Report the malaria status.
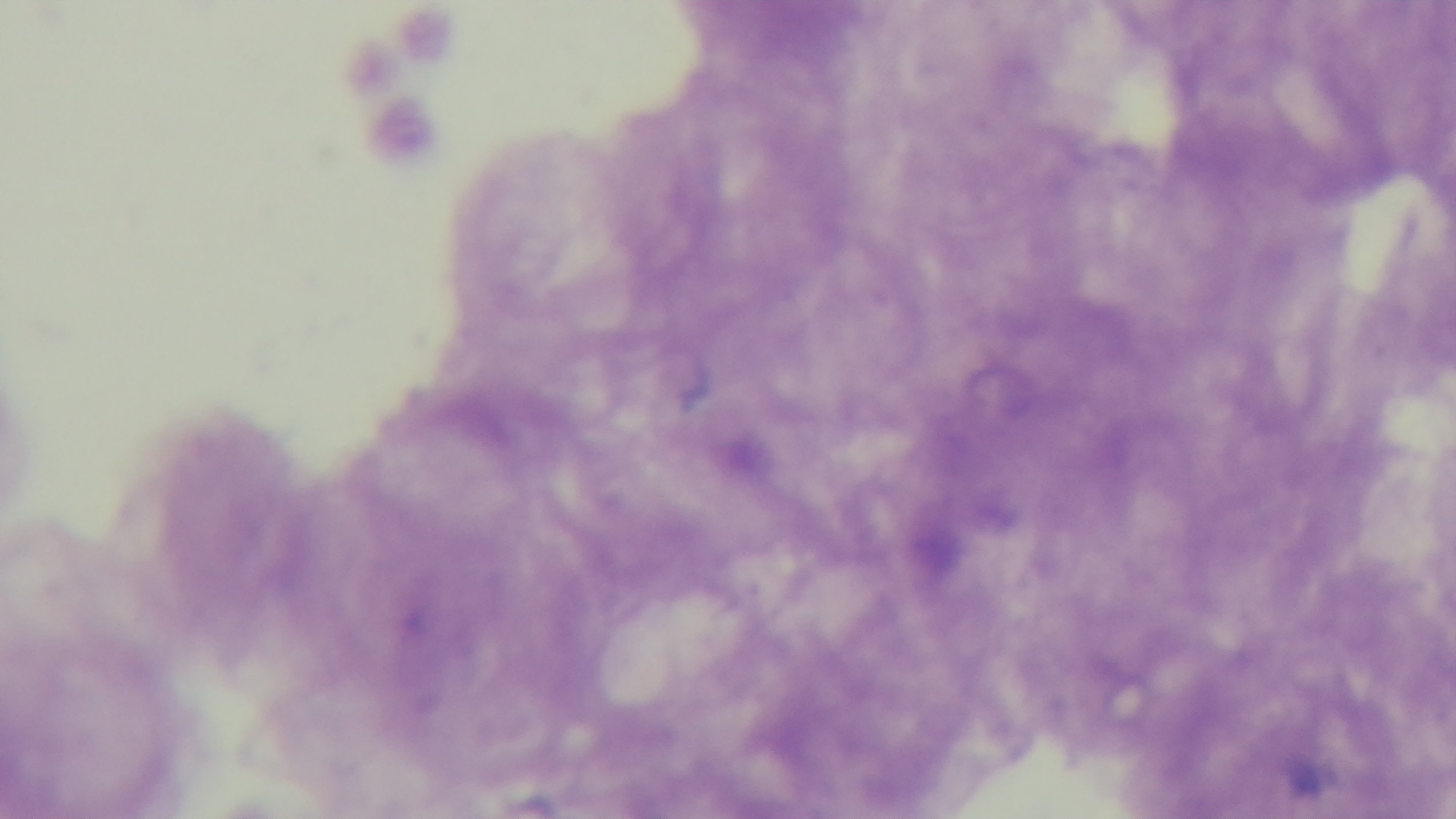
Negative.

Summary:
  - Preparation: thick
  - Modality: light microscopy
  - Stain: Giemsa
  - Capture: mounted 4K digital camera
  - Field of view: one from the slide
  - Objective: 100x oil immersion